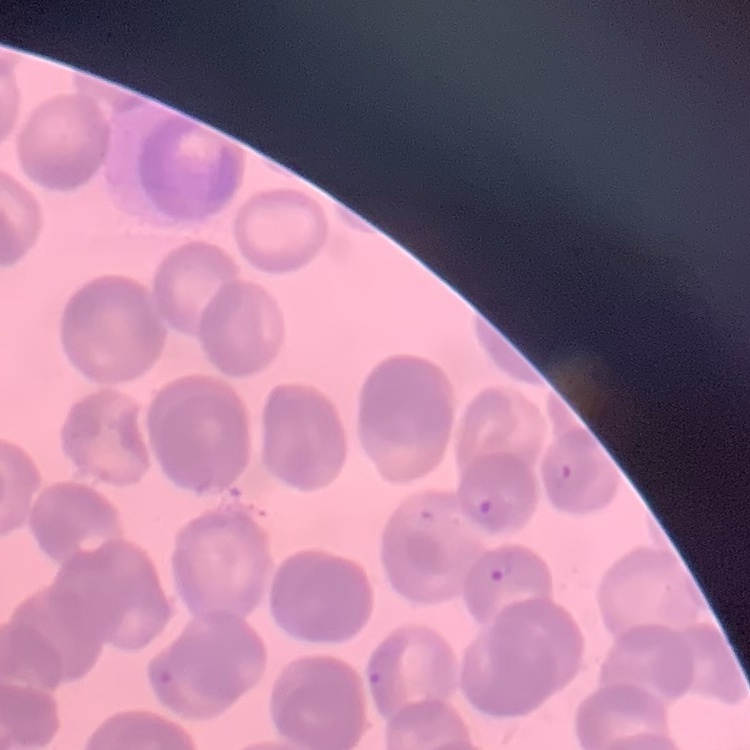

The erythrocytes exhibit rouleaux formation. One tile cut from a larger photomicrograph. Thin blood smear. Field's or Giemsa stain.